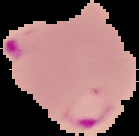

result = Plasmodium parasites identified
image size = 139×136 pixels
preparation = thin blood film
image type = segmented cell region with the area outside set to black